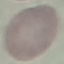

result: no malaria parasites seen
stain: Giemsa
capture: smartphone camera at the microscope eyepiece
image_type: automatically extracted cell patch, resized to 64 × 64 pixels
preparation: thin blood smear